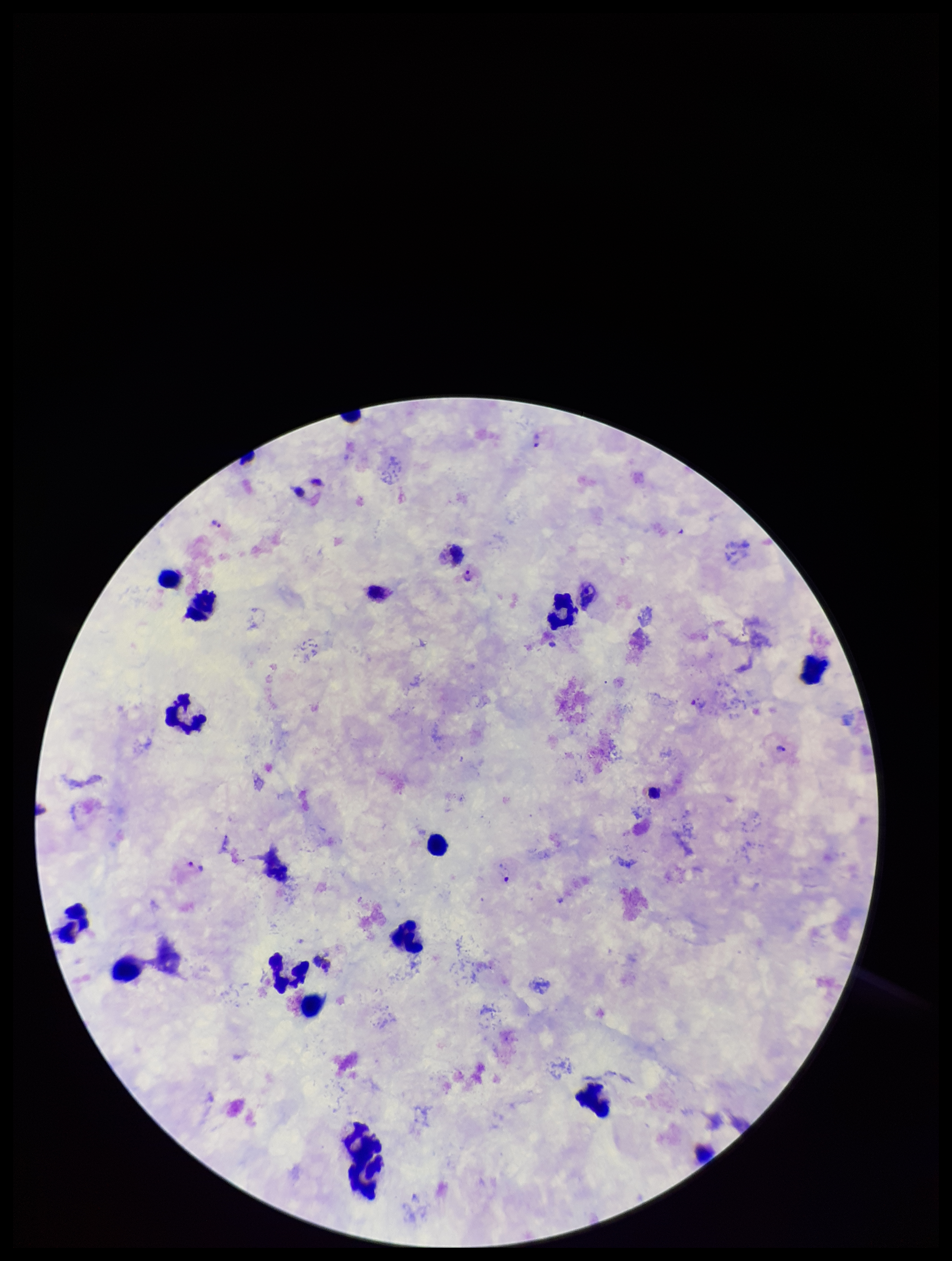

stain = Giemsa
preparation = thick blood smear
leukocyte count = 16
parasite count = 5
species reported for this patient = Plasmodium vivax
field of view = one from this slide
capture = smartphone photograph through the microscope eyepiece
patient malaria status = infected
image size = 952×1261 pixels
Plasmodium parasites = identified